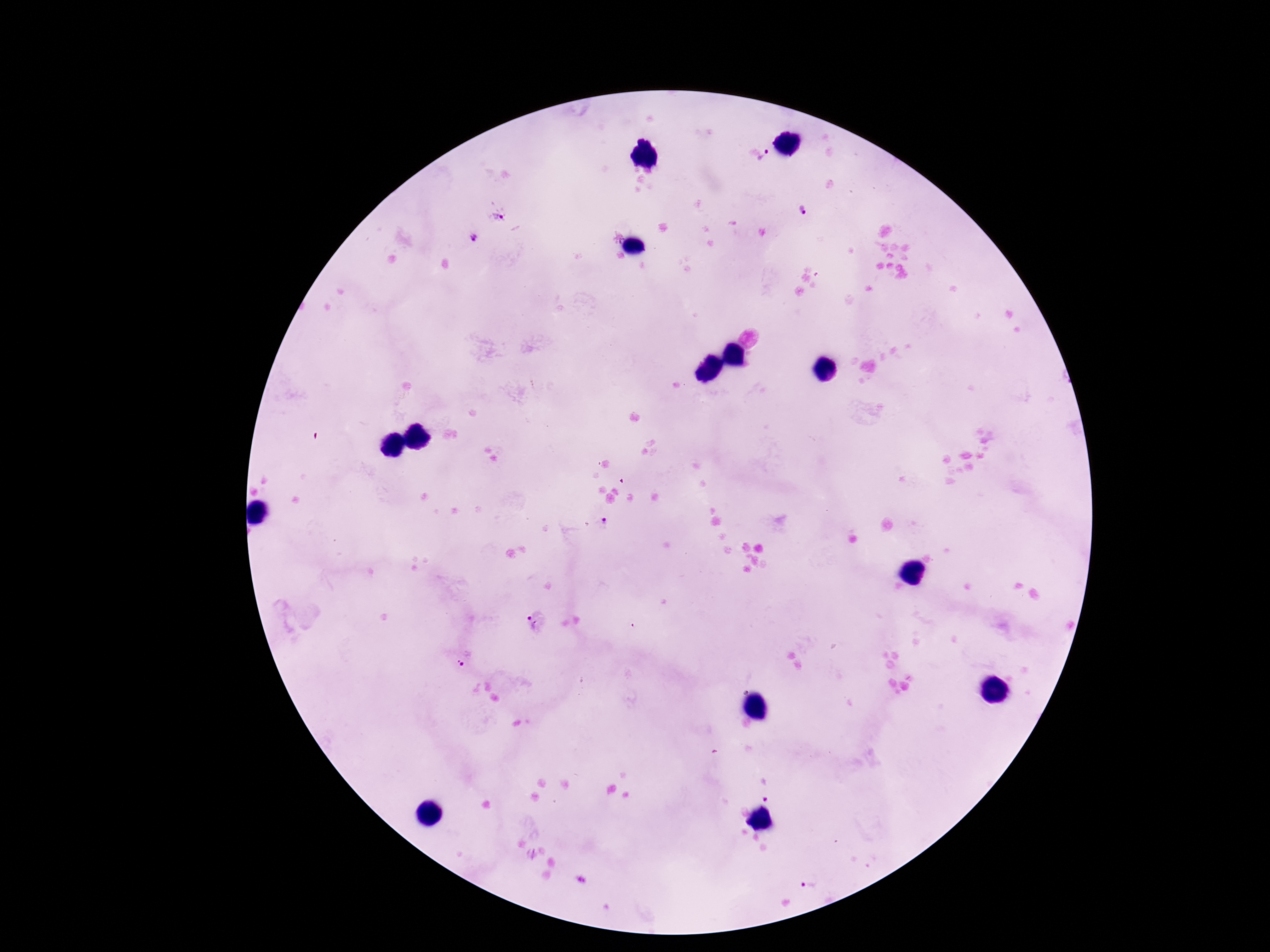
Approximate centers as (x, y) in pixels. Plasmodium parasite locations: (766, 158), (804, 211), (499, 216), (616, 236), (473, 238), (604, 524), (536, 621), (467, 660), (767, 789), (808, 885). Giemsa stain. Patient malaria status: positive. Image is 1270×952 pixels. 100x magnification. Thick peripheral-blood smear. One field from this slide. Photographed through the microscope eyepiece with a smartphone camera.